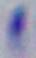

Photomicrograph. 1000x magnification. Toxoplasma gondii is shown.